State the blood parasite species.
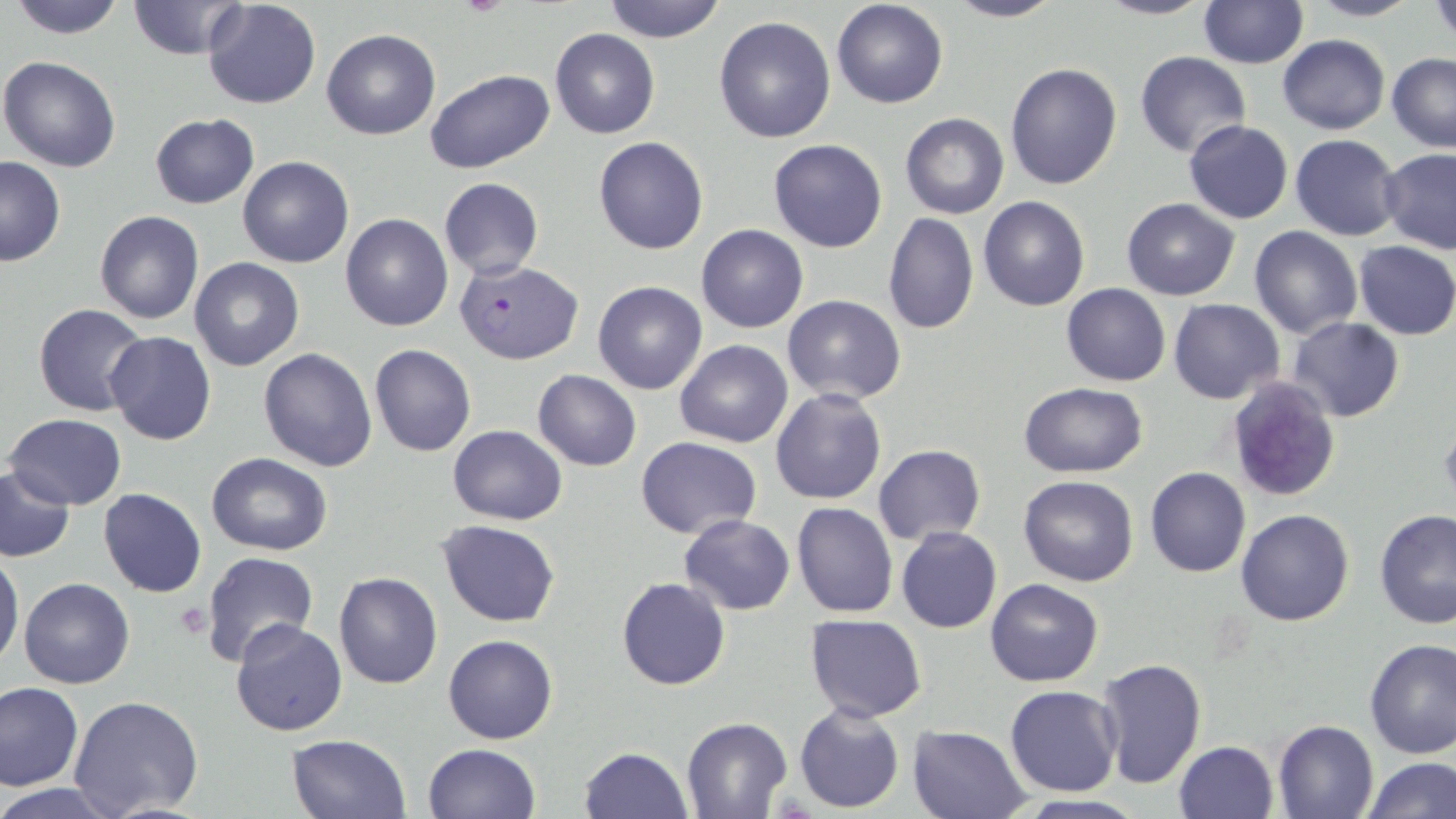

Plasmodium falciparum.

Approximate bounding boxes as named x1/y1/x2/y2 corners in pixels. Platelet locations: (x1=174, y1=603, x2=214, y2=639). Uninfected red blood cell locations: (x1=9, y1=0, x2=129, y2=38), (x1=128, y1=0, x2=253, y2=59), (x1=202, y1=0, x2=322, y2=110), (x1=600, y1=0, x2=729, y2=43), (x1=831, y1=0, x2=949, y2=108), (x1=943, y1=0, x2=1066, y2=23), (x1=1093, y1=0, x2=1217, y2=21), (x1=1305, y1=0, x2=1420, y2=21), (x1=1428, y1=0, x2=1456, y2=41), (x1=1198, y1=2, x2=1309, y2=68), (x1=713, y1=16, x2=837, y2=143), (x1=549, y1=28, x2=660, y2=138), (x1=322, y1=29, x2=440, y2=139), (x1=1276, y1=34, x2=1389, y2=134), (x1=1135, y1=52, x2=1252, y2=157), (x1=1386, y1=53, x2=1456, y2=153), (x1=0, y1=55, x2=122, y2=173), (x1=1004, y1=63, x2=1122, y2=190), (x1=424, y1=68, x2=555, y2=174), (x1=900, y1=112, x2=1009, y2=219), (x1=149, y1=113, x2=259, y2=208), (x1=1184, y1=120, x2=1293, y2=223), (x1=1290, y1=134, x2=1402, y2=240), (x1=594, y1=136, x2=709, y2=255), (x1=767, y1=138, x2=889, y2=253), (x1=1379, y1=148, x2=1456, y2=254), (x1=0, y1=157, x2=66, y2=267), (x1=237, y1=157, x2=353, y2=268), (x1=438, y1=177, x2=544, y2=278), (x1=979, y1=197, x2=1089, y2=311), (x1=1121, y1=198, x2=1241, y2=300), (x1=95, y1=211, x2=203, y2=325), (x1=883, y1=212, x2=980, y2=335), (x1=340, y1=213, x2=453, y2=331), (x1=695, y1=224, x2=809, y2=333), (x1=1249, y1=226, x2=1362, y2=338), (x1=1353, y1=240, x2=1456, y2=339), (x1=189, y1=257, x2=305, y2=371), (x1=592, y1=281, x2=708, y2=395), (x1=1061, y1=284, x2=1169, y2=386), (x1=782, y1=294, x2=908, y2=404), (x1=1168, y1=298, x2=1284, y2=404), (x1=34, y1=304, x2=149, y2=416), (x1=1286, y1=316, x2=1405, y2=422), (x1=104, y1=331, x2=216, y2=445), (x1=676, y1=340, x2=793, y2=448), (x1=368, y1=344, x2=477, y2=457), (x1=258, y1=347, x2=378, y2=471), (x1=532, y1=369, x2=641, y2=471), (x1=1225, y1=374, x2=1341, y2=503), (x1=1017, y1=383, x2=1147, y2=477), (x1=770, y1=388, x2=887, y2=506), (x1=6, y1=413, x2=127, y2=509), (x1=446, y1=425, x2=567, y2=524), (x1=636, y1=437, x2=763, y2=538), (x1=873, y1=445, x2=986, y2=545), (x1=207, y1=453, x2=332, y2=555), (x1=1, y1=466, x2=74, y2=560), (x1=1146, y1=467, x2=1250, y2=578), (x1=1018, y1=475, x2=1140, y2=586), (x1=99, y1=488, x2=206, y2=597), (x1=791, y1=502, x2=897, y2=618), (x1=1376, y1=508, x2=1456, y2=629), (x1=1235, y1=509, x2=1356, y2=627), (x1=678, y1=513, x2=795, y2=615), (x1=437, y1=520, x2=560, y2=627), (x1=896, y1=527, x2=1002, y2=633), (x1=0, y1=551, x2=24, y2=669), (x1=200, y1=552, x2=320, y2=671), (x1=332, y1=571, x2=443, y2=691), (x1=617, y1=576, x2=731, y2=690), (x1=20, y1=577, x2=134, y2=688), (x1=986, y1=578, x2=1103, y2=687), (x1=806, y1=615, x2=927, y2=721), (x1=228, y1=618, x2=347, y2=737), (x1=443, y1=634, x2=558, y2=743), (x1=1363, y1=638, x2=1456, y2=758), (x1=1094, y1=658, x2=1208, y2=792), (x1=0, y1=681, x2=83, y2=792), (x1=1005, y1=686, x2=1123, y2=797), (x1=68, y1=695, x2=203, y2=817), (x1=793, y1=704, x2=905, y2=813), (x1=681, y1=715, x2=792, y2=816), (x1=1271, y1=720, x2=1378, y2=819), (x1=907, y1=725, x2=1032, y2=819), (x1=286, y1=732, x2=410, y2=818), (x1=1173, y1=740, x2=1279, y2=819), (x1=422, y1=742, x2=540, y2=818), (x1=577, y1=747, x2=692, y2=819), (x1=1362, y1=755, x2=1454, y2=818), (x1=0, y1=783, x2=122, y2=818). Plasmodium falciparum-infected red blood cell locations: (x1=455, y1=259, x2=581, y2=363). One field of a larger specimen. Light microscopy. Image is 1456×819 pixels. Captured at 1000x magnification. Thin blood film. May-Grünwald-Giemsa stain.